Name the parasite shown.
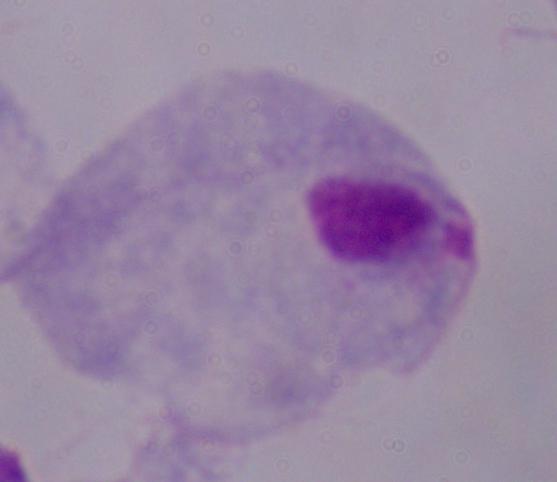
A trichomonad.

Micrograph. 1000x magnification.